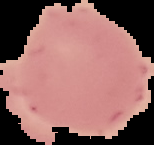

Image is 154×145 pixels. Cell region segmented out of the field of view; the surrounding area is masked to black. Result: no malaria parasites detected. From a thin blood film.